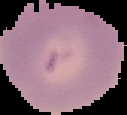

{
  "malaria_status": "uninfected",
  "image_size": "127×115 pixels",
  "image_type": "cell region segmented out of the field of view; surrounding area masked to black",
  "preparation": "thin blood smear"
}